Assess this cell for malaria.
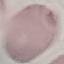
It is uninfected.

capture = smartphone through the microscope eyepiece
image type = cell patch, automatically extracted from a larger field of view and resized to 64 × 64 pixels
preparation = thin smear
stain = Giemsa